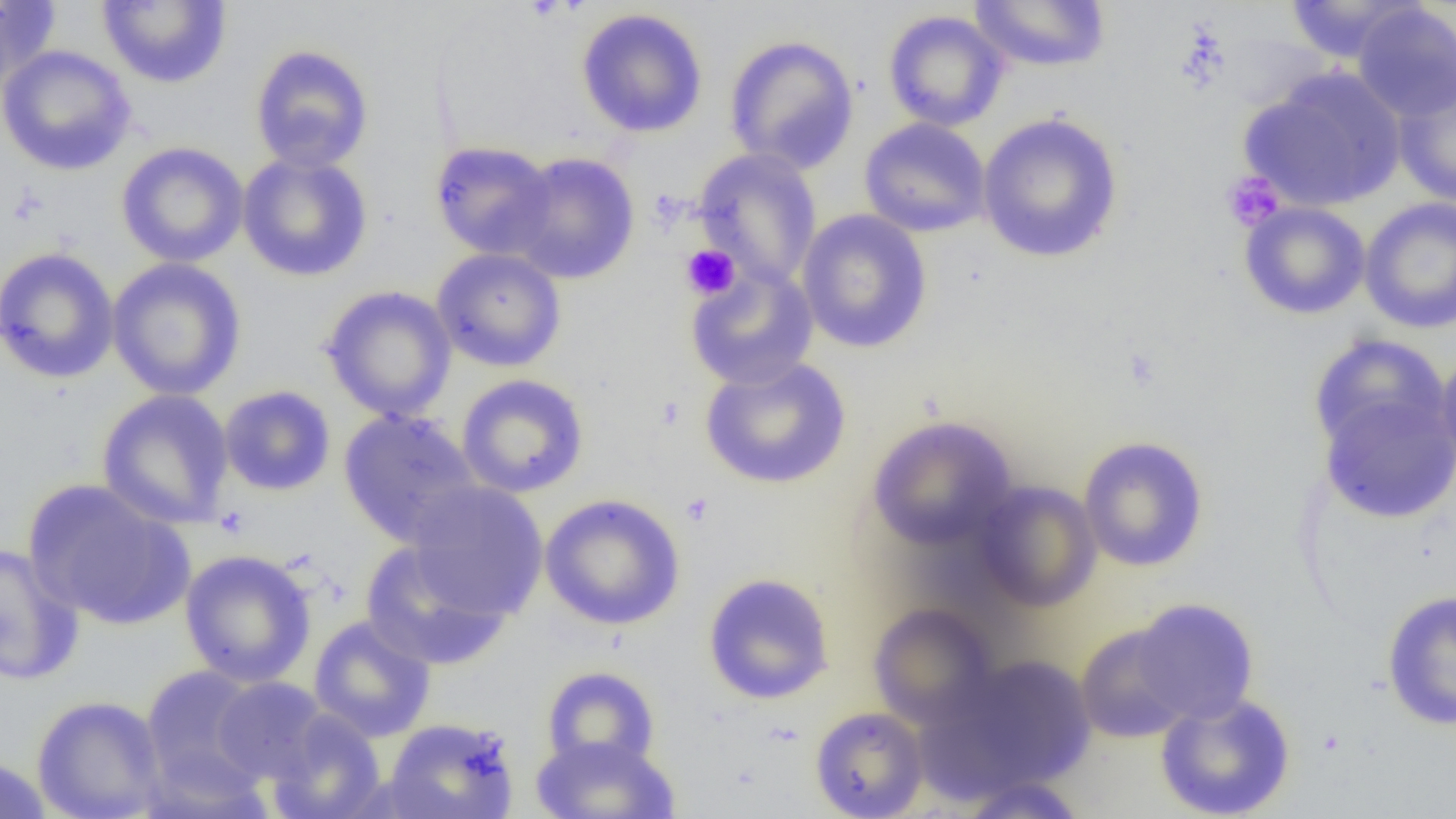 Approximate bounding boxes as (x1, y1, x2, y2) in pixels. Uninfected red blood cell locations: (0, 0, 61, 91), (97, 0, 232, 88), (969, 0, 1112, 73), (1282, 0, 1427, 64), (1352, 3, 1456, 121), (575, 8, 709, 138), (882, 10, 1010, 132), (723, 34, 860, 174), (249, 44, 374, 173), (0, 45, 137, 176), (1240, 68, 1406, 212), (1392, 73, 1456, 208), (977, 112, 1124, 264), (859, 118, 991, 238), (116, 141, 249, 268), (429, 141, 558, 260), (693, 148, 823, 287), (237, 152, 374, 282), (506, 152, 641, 284), (1359, 198, 1456, 334), (1239, 201, 1370, 320), (797, 209, 933, 354), (0, 247, 120, 384), (431, 248, 567, 372), (107, 258, 247, 401), (684, 263, 819, 391), (320, 285, 457, 422), (1308, 333, 1449, 460), (1434, 347, 1456, 479), (699, 355, 852, 490), (455, 374, 589, 498), (219, 385, 336, 497), (1319, 387, 1456, 524), (96, 388, 235, 529), (338, 408, 483, 547), (867, 415, 1018, 552), (1078, 435, 1209, 572), (23, 478, 194, 630), (404, 480, 548, 619), (972, 480, 1102, 611), (540, 493, 686, 631), (359, 539, 511, 671), (0, 542, 85, 686), (178, 549, 317, 687), (702, 572, 835, 705), (1381, 590, 1456, 731), (1130, 598, 1260, 724), (868, 602, 999, 730), (308, 615, 436, 742), (1075, 622, 1196, 744), (937, 653, 1097, 796), (140, 664, 268, 796), (540, 665, 660, 772), (211, 677, 329, 784), (1155, 691, 1296, 819), (31, 694, 168, 819), (810, 706, 929, 818), (266, 709, 387, 819), (383, 717, 520, 819), (530, 733, 681, 818), (0, 756, 53, 819), (959, 775, 1087, 818). Platelet locations: (1222, 171, 1285, 231), (681, 245, 741, 300), (653, 396, 685, 431), (680, 492, 715, 528), (214, 506, 250, 539). Slide-level diagnosis: no evidence of blood parasites. Image is 1456×819 pixels. 1000x magnification. Thin blood film. Optical microscopy. Single field of view.